Report the malaria status of this cell.
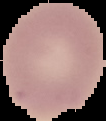
It is uninfected.

Image is 106×121 pixels. Cell region segmented out of the field of view; the surrounding area is masked to black. From a thin blood smear.